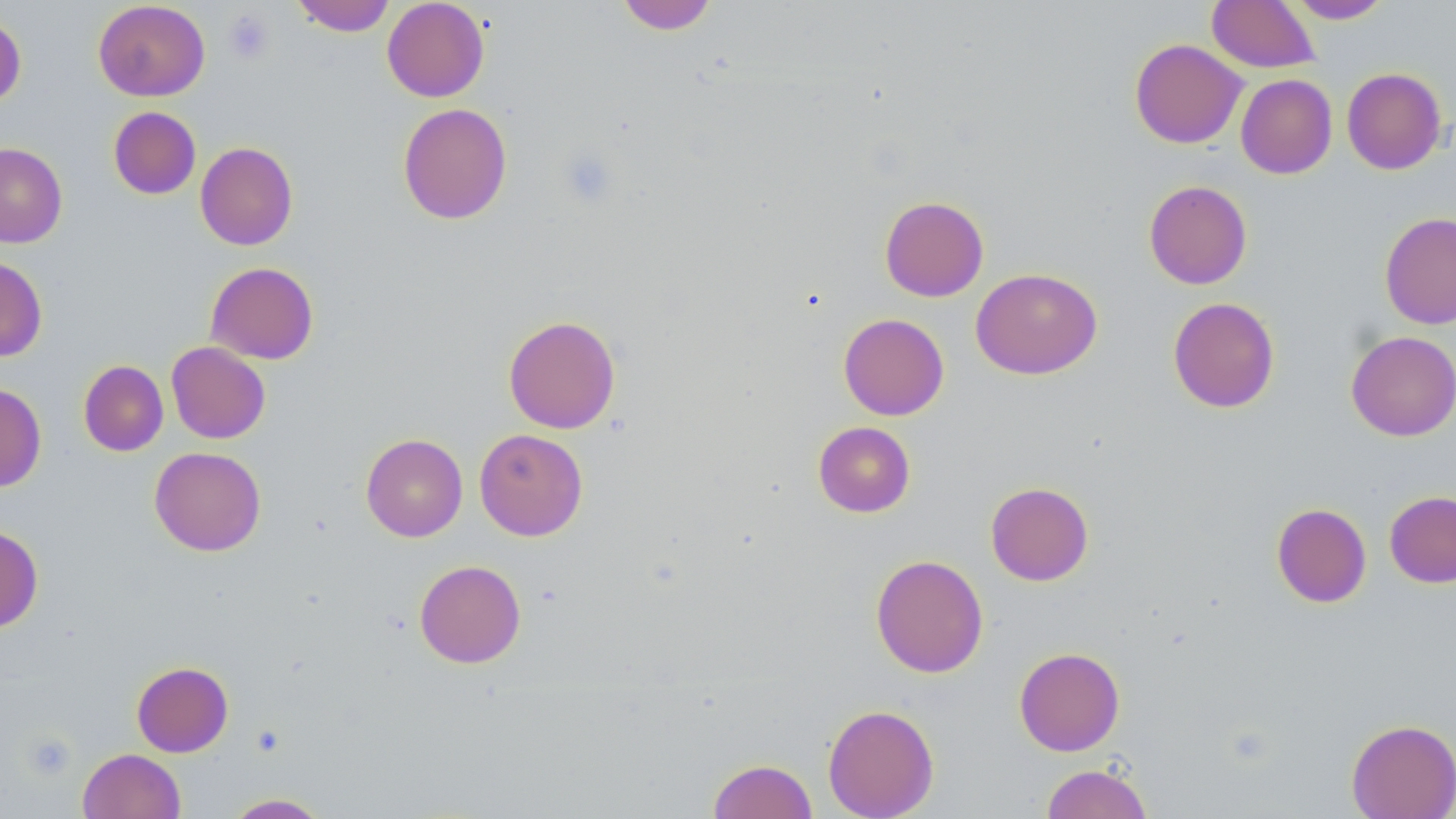
Approximate bounding boxes as named x1/y1/x2/y2 corners in pixels. Uninfected red blood cell locations: (x1=290, y1=0, x2=396, y2=36), (x1=382, y1=0, x2=489, y2=102), (x1=617, y1=0, x2=717, y2=34), (x1=1207, y1=0, x2=1320, y2=73), (x1=1286, y1=0, x2=1393, y2=23), (x1=93, y1=1, x2=210, y2=101), (x1=0, y1=13, x2=26, y2=108), (x1=1129, y1=39, x2=1247, y2=149), (x1=1341, y1=67, x2=1447, y2=175), (x1=1235, y1=74, x2=1337, y2=178), (x1=397, y1=102, x2=513, y2=225), (x1=108, y1=106, x2=201, y2=199), (x1=195, y1=141, x2=298, y2=250), (x1=0, y1=143, x2=68, y2=248), (x1=1143, y1=179, x2=1252, y2=290), (x1=879, y1=195, x2=989, y2=302), (x1=1379, y1=211, x2=1456, y2=330), (x1=0, y1=256, x2=48, y2=362), (x1=205, y1=261, x2=319, y2=364), (x1=971, y1=267, x2=1102, y2=380), (x1=1167, y1=297, x2=1280, y2=413), (x1=838, y1=313, x2=949, y2=420), (x1=503, y1=314, x2=621, y2=434), (x1=1346, y1=331, x2=1456, y2=441), (x1=166, y1=342, x2=270, y2=443), (x1=78, y1=360, x2=168, y2=456), (x1=0, y1=383, x2=46, y2=492), (x1=813, y1=421, x2=916, y2=517), (x1=474, y1=428, x2=588, y2=541), (x1=361, y1=433, x2=467, y2=542), (x1=149, y1=447, x2=266, y2=556), (x1=985, y1=481, x2=1094, y2=586), (x1=1385, y1=490, x2=1456, y2=588), (x1=1271, y1=503, x2=1372, y2=608), (x1=0, y1=525, x2=43, y2=633), (x1=870, y1=554, x2=989, y2=678), (x1=414, y1=559, x2=526, y2=668), (x1=1014, y1=647, x2=1125, y2=756), (x1=131, y1=661, x2=233, y2=757), (x1=822, y1=703, x2=939, y2=818), (x1=1346, y1=718, x2=1456, y2=818), (x1=78, y1=748, x2=186, y2=819), (x1=707, y1=759, x2=818, y2=819), (x1=1040, y1=763, x2=1154, y2=819), (x1=223, y1=792, x2=332, y2=818). Platelet locations: (x1=224, y1=10, x2=274, y2=63), (x1=558, y1=147, x2=619, y2=207), (x1=21, y1=732, x2=75, y2=781). Slide-level diagnosis: no evidence of blood parasites. May-Grünwald-Giemsa-stained preparation. Thin blood film. Captured at 1000x magnification. Image is 1456×819 pixels. Optical microscopy. Single field of view.